Assess this cell for malaria.
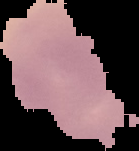

Uninfected.

Cell region segmented out of the field of view; the surrounding area is masked to black. From a thin blood smear. Image is 139×151 pixels.